Name the cell type shown.
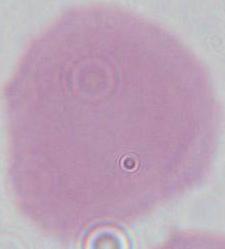
An erythrocyte.

Summary:
  - Modality: micrograph
  - Magnification: 1000x